Locate every Plasmodium parasite.
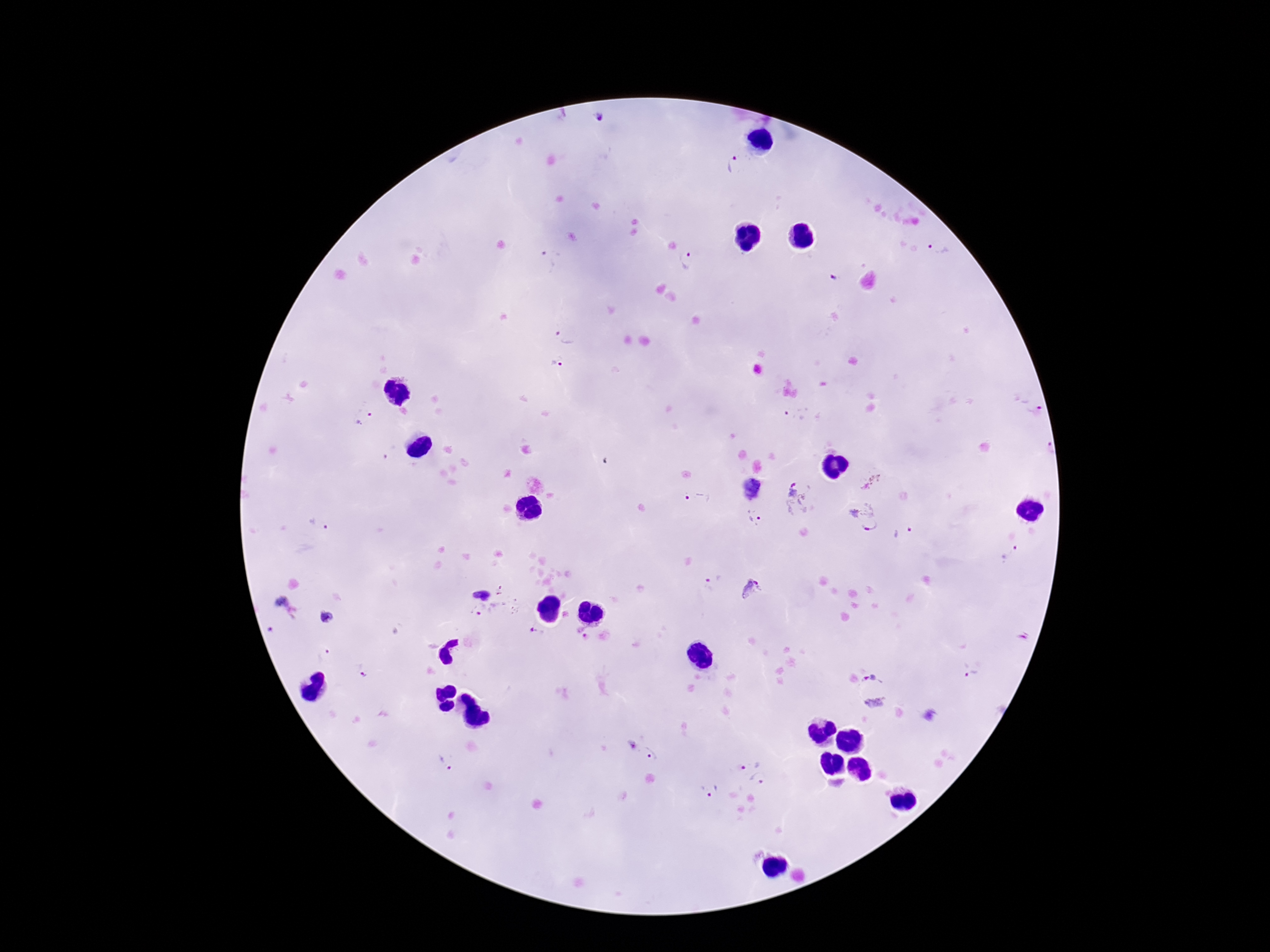
Approximate object centers, in pixels from the top-left corner.
Plasmodium parasites: (x=599, y=120), (x=733, y=164), (x=940, y=246), (x=552, y=259), (x=689, y=261), (x=835, y=277), (x=566, y=336), (x=557, y=368), (x=800, y=413), (x=365, y=418), (x=391, y=453), (x=872, y=482), (x=752, y=490), (x=799, y=497), (x=697, y=498), (x=862, y=517), (x=755, y=518), (x=319, y=526), (x=903, y=533), (x=1012, y=554), (x=712, y=575), (x=480, y=588), (x=750, y=588), (x=500, y=591), (x=285, y=608), (x=495, y=615), (x=329, y=619), (x=536, y=632), (x=582, y=633), (x=322, y=655), (x=874, y=673), (x=970, y=673), (x=366, y=676), (x=875, y=703), (x=632, y=744), (x=652, y=756), (x=750, y=761), (x=443, y=765), (x=758, y=780), (x=709, y=791).

Summary:
  - Preparation: thick blood film
  - Patient malaria status: infected
  - Capture: smartphone camera through the microscope eyepiece
  - Stain: Giemsa
  - Image size: 1270×952 pixels
  - Field of view: one from this slide
  - Magnification: 100x